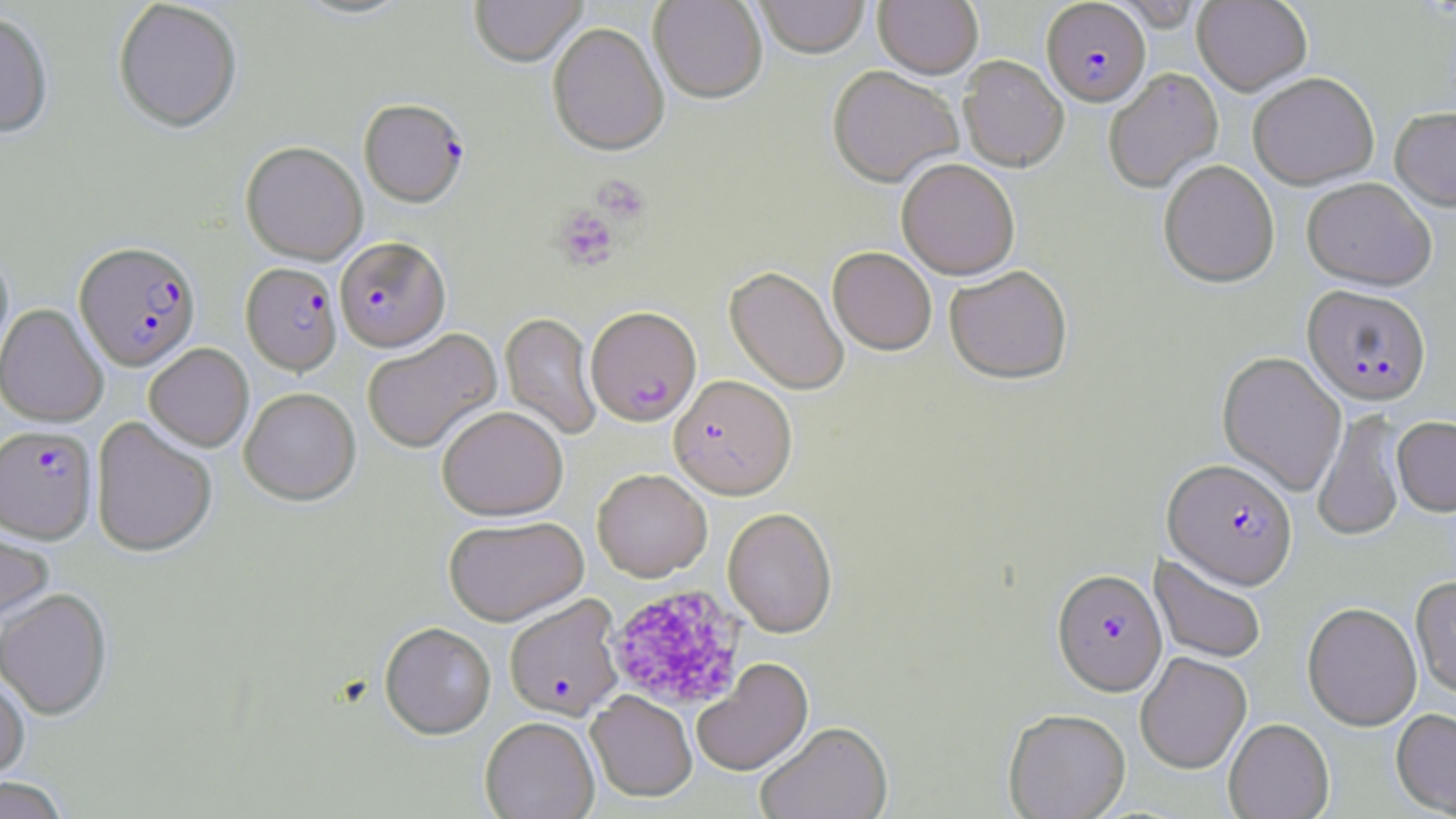

Approximate bounding boxes as named x1/y1/x2/y2 corners in pixels. Uninfected red blood cell locations: (x1=292, y1=0, x2=415, y2=22), (x1=469, y1=0, x2=588, y2=69), (x1=649, y1=0, x2=768, y2=105), (x1=755, y1=0, x2=870, y2=61), (x1=873, y1=0, x2=983, y2=81), (x1=1193, y1=0, x2=1312, y2=96), (x1=113, y1=1, x2=242, y2=134), (x1=0, y1=12, x2=54, y2=139), (x1=548, y1=24, x2=669, y2=158), (x1=958, y1=57, x2=1068, y2=172), (x1=826, y1=68, x2=963, y2=190), (x1=1103, y1=68, x2=1223, y2=194), (x1=1248, y1=74, x2=1379, y2=190), (x1=1390, y1=108, x2=1456, y2=213), (x1=241, y1=142, x2=367, y2=265), (x1=896, y1=159, x2=1019, y2=280), (x1=1158, y1=160, x2=1279, y2=289), (x1=1302, y1=178, x2=1436, y2=291), (x1=827, y1=247, x2=937, y2=356), (x1=0, y1=248, x2=14, y2=375), (x1=724, y1=266, x2=849, y2=396), (x1=944, y1=266, x2=1073, y2=386), (x1=0, y1=304, x2=108, y2=427), (x1=500, y1=312, x2=602, y2=440), (x1=362, y1=329, x2=502, y2=454), (x1=144, y1=343, x2=253, y2=451), (x1=1217, y1=351, x2=1346, y2=496), (x1=239, y1=388, x2=360, y2=506), (x1=437, y1=406, x2=568, y2=521), (x1=1313, y1=408, x2=1407, y2=543), (x1=91, y1=416, x2=217, y2=557), (x1=1392, y1=416, x2=1456, y2=516), (x1=592, y1=468, x2=711, y2=581), (x1=722, y1=507, x2=837, y2=638), (x1=443, y1=515, x2=589, y2=626), (x1=0, y1=522, x2=54, y2=628), (x1=1150, y1=554, x2=1267, y2=664), (x1=1410, y1=577, x2=1456, y2=700), (x1=0, y1=588, x2=112, y2=720), (x1=1302, y1=602, x2=1422, y2=731), (x1=380, y1=622, x2=496, y2=740), (x1=1136, y1=652, x2=1252, y2=773), (x1=693, y1=658, x2=814, y2=777), (x1=0, y1=671, x2=30, y2=783), (x1=587, y1=691, x2=698, y2=803), (x1=1003, y1=708, x2=1131, y2=819), (x1=1391, y1=708, x2=1456, y2=817), (x1=480, y1=717, x2=599, y2=819), (x1=1224, y1=718, x2=1334, y2=819), (x1=755, y1=722, x2=893, y2=819), (x1=0, y1=777, x2=70, y2=819). Plasmodium falciparum-infected red blood cell locations: (x1=1041, y1=1, x2=1151, y2=107), (x1=358, y1=99, x2=468, y2=208), (x1=334, y1=237, x2=450, y2=352), (x1=74, y1=241, x2=201, y2=371), (x1=241, y1=263, x2=342, y2=376), (x1=1302, y1=285, x2=1432, y2=406), (x1=586, y1=306, x2=702, y2=427), (x1=669, y1=375, x2=796, y2=499), (x1=0, y1=426, x2=97, y2=543), (x1=1162, y1=458, x2=1298, y2=590), (x1=1052, y1=569, x2=1167, y2=697), (x1=504, y1=594, x2=624, y2=719). Platelet locations: (x1=592, y1=174, x2=651, y2=225), (x1=553, y1=205, x2=620, y2=271), (x1=606, y1=584, x2=747, y2=710). Slide-level diagnosis: Plasmodium falciparum. Thin blood smear. Light microscopy. Single field of view. May-Grünwald-Giemsa stain. Captured at 1000x magnification. Image is 1456×819 pixels.